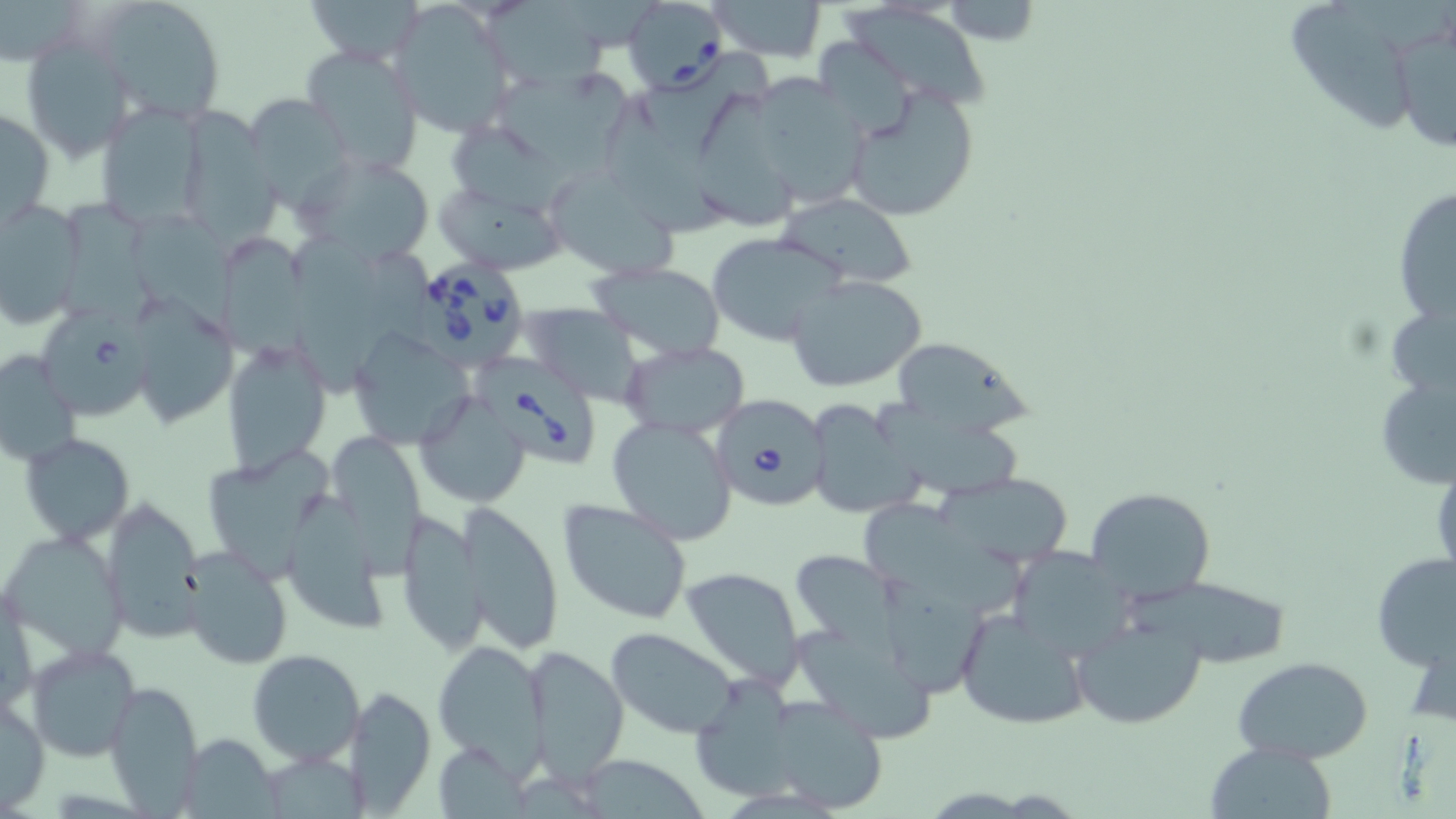
slide-level diagnosis = Babesia divergens
modality = optical microscopy
preparation = thin blood smear
image size = 1456×819 pixels
uninfected red blood cell locations = approximate bounding boxes as [x1, y1, x2, y2] in pixels: [97, 0, 227, 124], [302, 0, 426, 64], [708, 0, 828, 62], [937, 2, 1045, 45], [388, 4, 515, 138], [474, 4, 612, 96], [1293, 8, 1411, 135], [844, 9, 991, 115], [1390, 15, 1456, 159], [21, 34, 134, 161], [819, 37, 913, 139], [300, 44, 424, 173], [489, 66, 630, 166], [744, 74, 873, 210], [845, 87, 981, 222], [243, 92, 354, 203], [598, 98, 737, 250], [694, 100, 805, 231], [96, 102, 210, 230], [0, 104, 55, 231], [447, 123, 595, 213], [288, 152, 439, 271], [542, 164, 679, 279], [434, 179, 567, 274], [1391, 185, 1456, 332], [776, 191, 920, 289], [54, 192, 160, 331], [0, 199, 84, 330], [131, 210, 250, 349], [708, 233, 844, 345], [215, 234, 313, 374], [274, 236, 402, 398], [589, 261, 727, 359], [788, 274, 928, 393], [132, 299, 236, 428], [519, 304, 644, 403], [349, 327, 474, 449], [897, 339, 1029, 440], [221, 340, 331, 474], [620, 341, 749, 438], [0, 351, 79, 470], [1374, 369, 1456, 492], [416, 392, 531, 506], [873, 395, 1026, 503], [803, 398, 919, 521], [607, 413, 739, 547], [331, 431, 424, 587], [21, 433, 134, 546], [202, 451, 339, 588], [942, 473, 1074, 568], [1084, 487, 1215, 603], [284, 490, 384, 639], [556, 497, 694, 625], [100, 500, 206, 640], [858, 503, 1035, 619], [462, 505, 565, 654], [395, 509, 487, 655], [3, 530, 127, 659], [182, 545, 294, 670], [1006, 546, 1135, 664], [791, 548, 901, 644], [1371, 553, 1456, 671], [681, 566, 806, 687], [1133, 574, 1295, 668], [874, 577, 995, 703], [955, 605, 1091, 731], [1070, 613, 1206, 729], [607, 628, 741, 739], [793, 629, 945, 749], [432, 639, 549, 767], [26, 643, 142, 763], [524, 646, 630, 777], [248, 649, 365, 765], [1233, 655, 1373, 762], [697, 679, 803, 799], [105, 681, 204, 810], [342, 687, 436, 812], [751, 690, 891, 814], [0, 693, 49, 812], [176, 733, 280, 817], [1203, 743, 1338, 818], [266, 748, 373, 819], [576, 752, 713, 819]
Babesia divergens-infected red blood cell locations = approximate bounding boxes as [x1, y1, x2, y2] in pixels: [621, 0, 727, 92], [420, 259, 527, 370], [36, 305, 163, 434], [476, 359, 597, 469], [709, 395, 830, 511]
field of view = one of a larger specimen
stain = May-Grünwald-Giemsa
magnification = 1000x